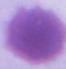 An erythrocyte is seen. Micrograph. 1000x magnification.